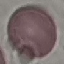

{
  "result": "no malaria parasites seen",
  "stain": "Giemsa",
  "preparation": "thin blood smear",
  "image_type": "cell patch, automatically extracted from a larger field of view and resized to 64 × 64 pixels",
  "capture": "smartphone camera at the microscope eyepiece"
}